Classify this cell by malaria status.
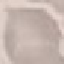
It is uninfected.

Giemsa stain. Thin smear of blood. Automatically extracted cell patch, resized to 64 × 64 pixels. Acquired by smartphone through the microscope eyepiece.